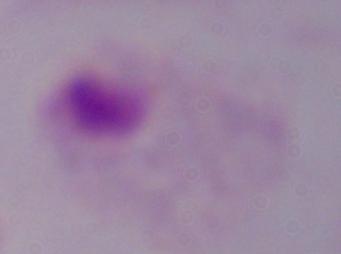
Summary:
  - Magnification: 1000x
  - Identification: trichomonad
  - Modality: micrograph